Draw a bounding box around every parasitised red blood cell, every trophozoite, every gametocyte, every leukocyte, and every artifact (platelet-like body, stain precipitate, or debris).
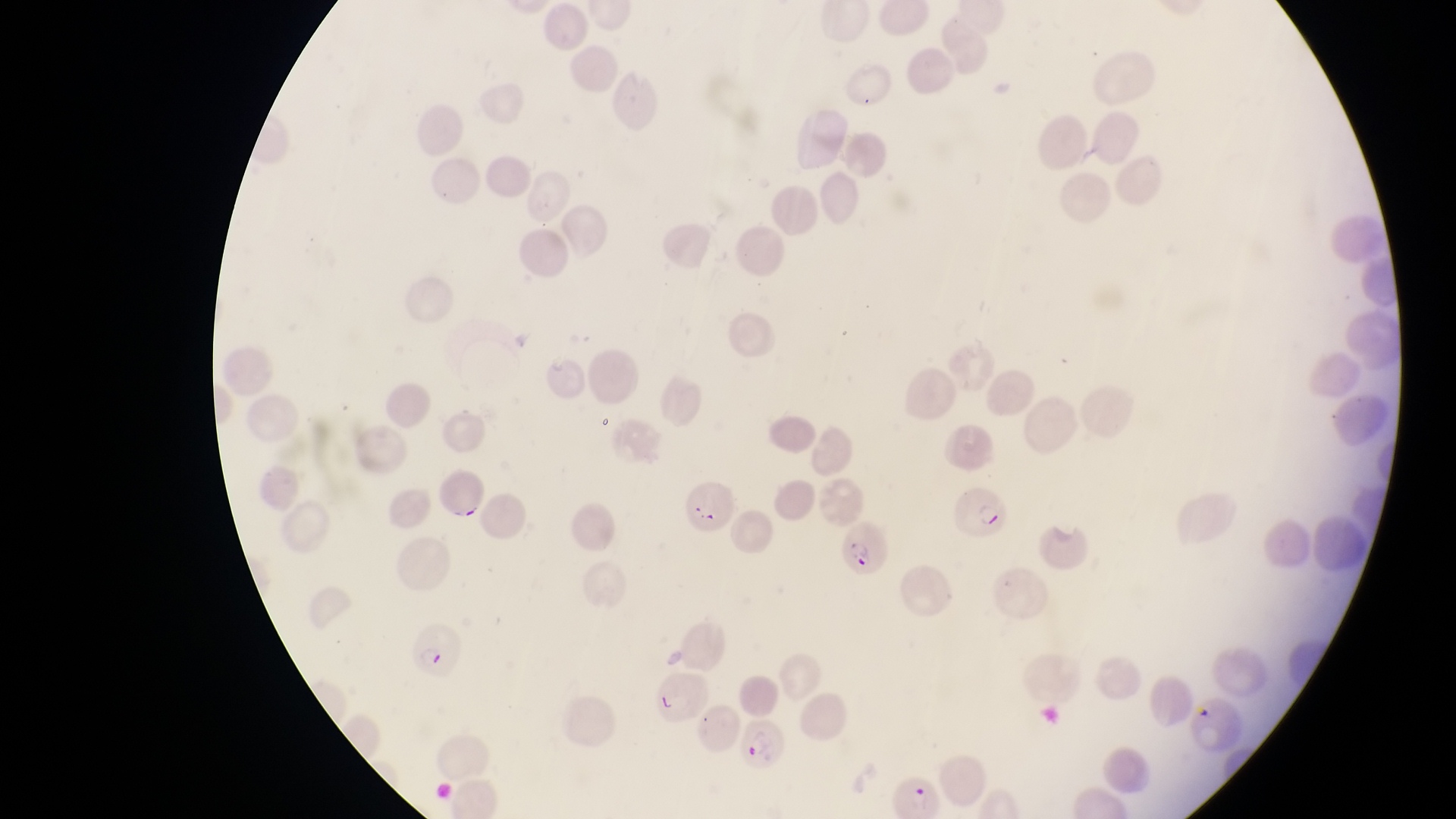
Approximate bounding boxes as left top right bottom in pixels.
Parasitised red blood cells: 682 478 735 537; 954 478 1012 544; 836 513 891 580; 406 618 467 677; 742 719 791 771; 893 770 946 816.
No leukocytes observed.

field of view = single
magnification = 1000x
preparation = thin blood film
country = Uganda
image size = 1456×819 pixels
capture = smartphone photograph through the eyepiece of an Olympus CX-23 microscope